Locate and identify every blood parasite.
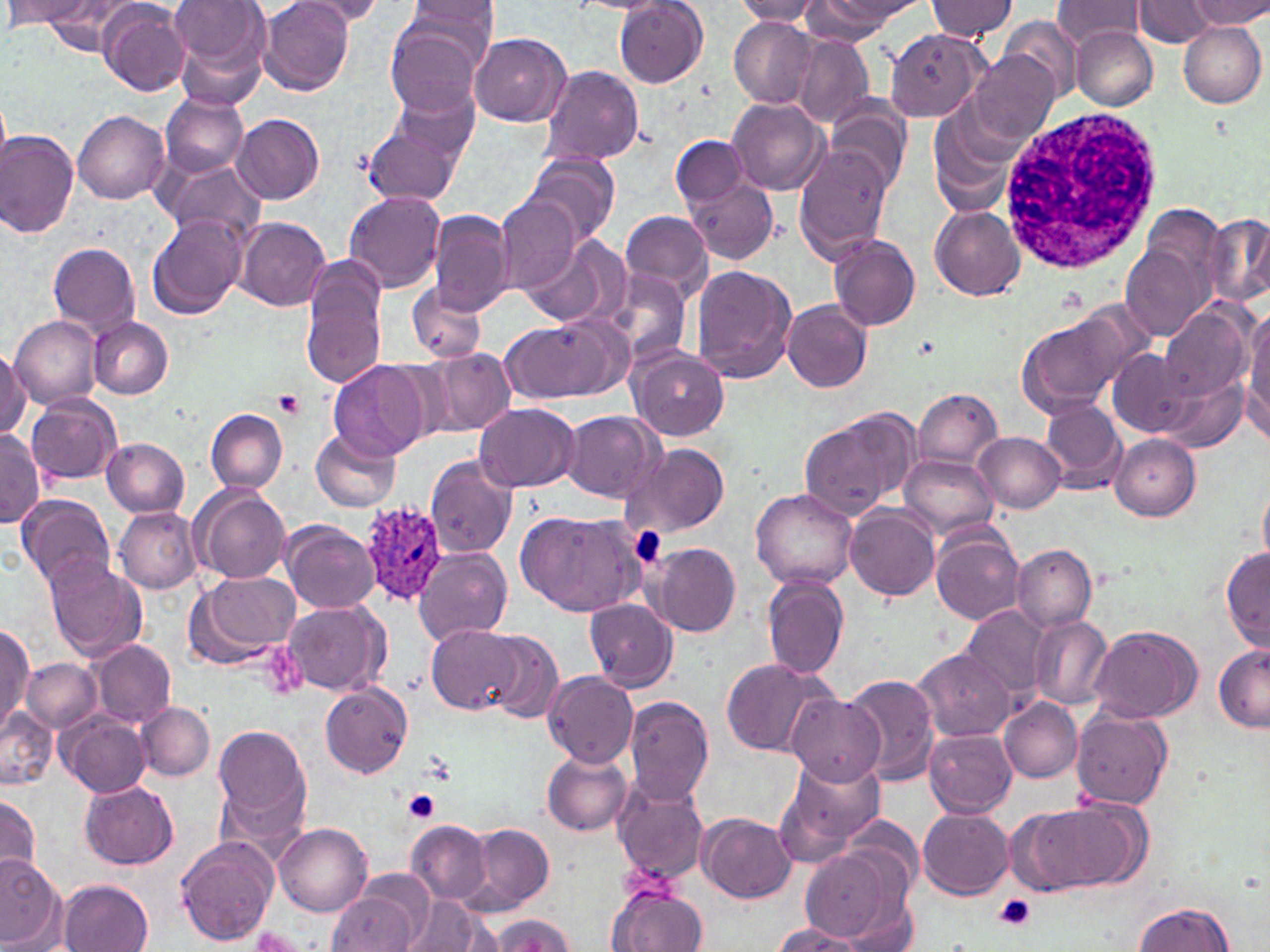
Approximate bounding boxes as (x1, y1, x2, y2) in pixels.
Plasmodium ovale-infected red blood cells: (359, 500, 452, 606).
No Plasmodium falciparum, Plasmodium malariae, Plasmodium vivax, Babesia divergens, or Trypanosoma brucei observed.

Summary:
  - Platelet locations: (274, 389, 305, 418), (404, 789, 440, 821), (994, 894, 1037, 932)
  - Uninfected red blood cell locations: (7, 0, 93, 25), (169, 0, 266, 70), (259, 0, 354, 97), (397, 0, 500, 74), (806, 0, 917, 36), (926, 0, 1018, 42), (1050, 0, 1147, 49), (1133, 0, 1215, 47), (1190, 0, 1270, 29), (292, 1, 390, 26), (614, 1, 708, 88), (734, 1, 825, 25), (39, 2, 141, 53), (98, 3, 191, 96), (999, 16, 1082, 100), (728, 18, 817, 108), (385, 21, 485, 118), (1178, 22, 1266, 107), (1071, 26, 1158, 110), (886, 29, 988, 120), (470, 33, 570, 126), (793, 35, 875, 129), (969, 51, 1059, 145), (540, 64, 645, 167), (390, 81, 480, 163), (159, 92, 248, 178), (0, 98, 11, 172), (727, 98, 829, 196), (825, 100, 911, 192), (73, 111, 170, 204), (233, 113, 324, 205), (361, 119, 459, 207), (931, 122, 1013, 217), (0, 131, 79, 238), (669, 134, 748, 208), (794, 147, 895, 261), (523, 154, 619, 246), (157, 158, 265, 243), (684, 175, 780, 263), (343, 191, 447, 293), (495, 196, 581, 294), (929, 203, 1025, 300), (1141, 203, 1228, 293), (428, 210, 513, 315), (619, 211, 713, 298), (147, 214, 249, 320), (1202, 215, 1270, 308), (235, 218, 330, 311), (521, 234, 631, 331), (828, 236, 921, 331), (1122, 241, 1214, 341), (48, 242, 142, 341), (299, 258, 389, 390), (689, 266, 797, 383), (602, 269, 694, 370), (406, 282, 486, 362), (782, 300, 874, 394), (1014, 303, 1151, 420), (1244, 304, 1270, 432), (1157, 305, 1252, 403), (8, 313, 101, 410), (500, 315, 630, 406), (90, 317, 174, 399), (422, 346, 518, 439), (0, 347, 29, 438), (628, 347, 730, 441), (1107, 348, 1193, 437), (328, 361, 427, 462), (1158, 372, 1247, 451), (913, 387, 1002, 473), (26, 394, 121, 485), (906, 394, 1027, 537), (1038, 399, 1130, 494), (473, 402, 580, 492), (205, 408, 289, 494), (564, 411, 661, 501), (799, 415, 911, 521), (312, 429, 401, 512), (0, 430, 43, 528), (975, 432, 1066, 513), (1109, 435, 1199, 520), (102, 438, 190, 517), (622, 443, 733, 540), (900, 452, 998, 543), (425, 456, 517, 560), (1258, 479, 1270, 569), (191, 485, 290, 584), (750, 488, 859, 590), (18, 494, 117, 594), (845, 505, 940, 598), (114, 507, 202, 594), (519, 507, 644, 617), (87, 517, 188, 624), (281, 521, 382, 613), (931, 526, 1025, 624), (647, 543, 741, 638), (1011, 544, 1096, 633), (1220, 547, 1270, 649), (413, 548, 512, 646), (45, 560, 149, 663), (187, 571, 301, 669), (762, 576, 848, 679), (280, 598, 389, 697), (586, 599, 677, 691), (958, 603, 1052, 703), (1028, 615, 1113, 709), (0, 625, 34, 732), (427, 625, 522, 715), (1088, 625, 1203, 723), (481, 632, 562, 723), (91, 640, 176, 727), (1213, 644, 1270, 733), (912, 648, 1015, 741), (720, 657, 835, 758), (25, 658, 99, 732), (543, 670, 639, 767), (843, 672, 941, 785), (320, 683, 413, 778), (785, 694, 888, 784), (623, 695, 715, 808), (1001, 698, 1083, 782), (137, 702, 213, 781), (1, 705, 58, 789), (1070, 707, 1171, 807), (59, 711, 149, 796), (214, 724, 312, 830), (925, 729, 1016, 818), (542, 750, 632, 835), (773, 757, 885, 863), (613, 779, 708, 884), (79, 781, 178, 870), (0, 792, 43, 881), (1011, 801, 1139, 896), (917, 808, 1013, 898), (697, 812, 795, 902), (275, 821, 371, 916), (408, 821, 492, 907), (468, 824, 554, 911), (176, 836, 277, 946), (801, 849, 902, 943), (0, 854, 65, 949), (56, 879, 153, 952), (609, 885, 706, 952), (327, 890, 419, 952), (402, 897, 491, 949), (837, 898, 919, 952), (1133, 901, 1234, 952), (488, 914, 573, 952), (770, 922, 865, 952)
  - White blood cell locations: (1001, 106, 1163, 271)
  - Slide-level diagnosis: Plasmodium ovale
  - Preparation: thin blood film
  - Modality: light microscopy
  - Field of view: single
  - Stain: May-Grünwald-Giemsa
  - Image size: 1270×952 pixels
  - Magnification: 1000x